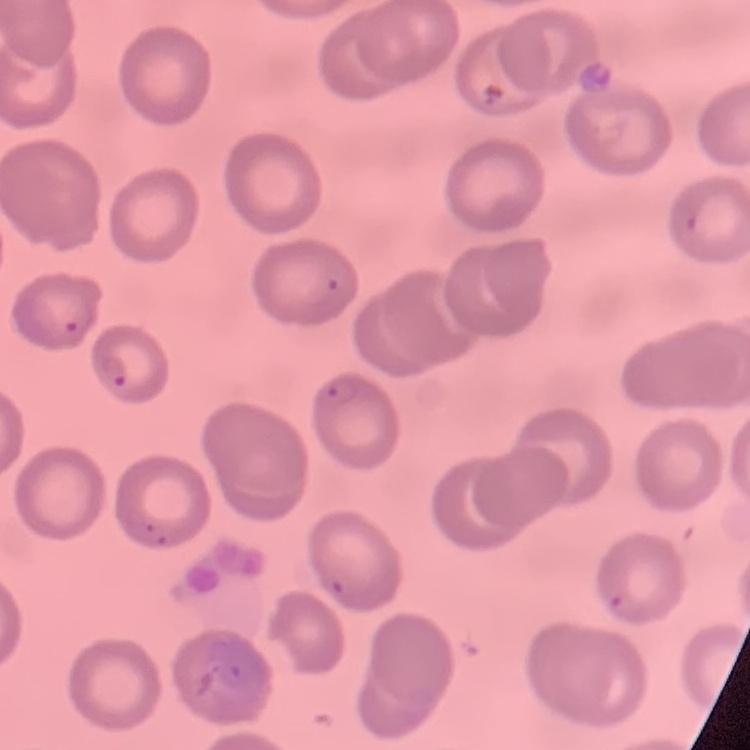
Summary:
  - Erythrocyte morphology: no rouleaux formation
  - Preparation: thin blood smear
  - Image type: square crop of a larger photomicrograph
  - Stain: Field's or Giemsa